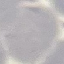
Malaria status: uninfected. Giemsa-stained preparation. Automatically extracted cell patch, resized to 64 × 64 pixels. Thin blood film. Acquired by smartphone through the microscope eyepiece.